Identify the preparation type.
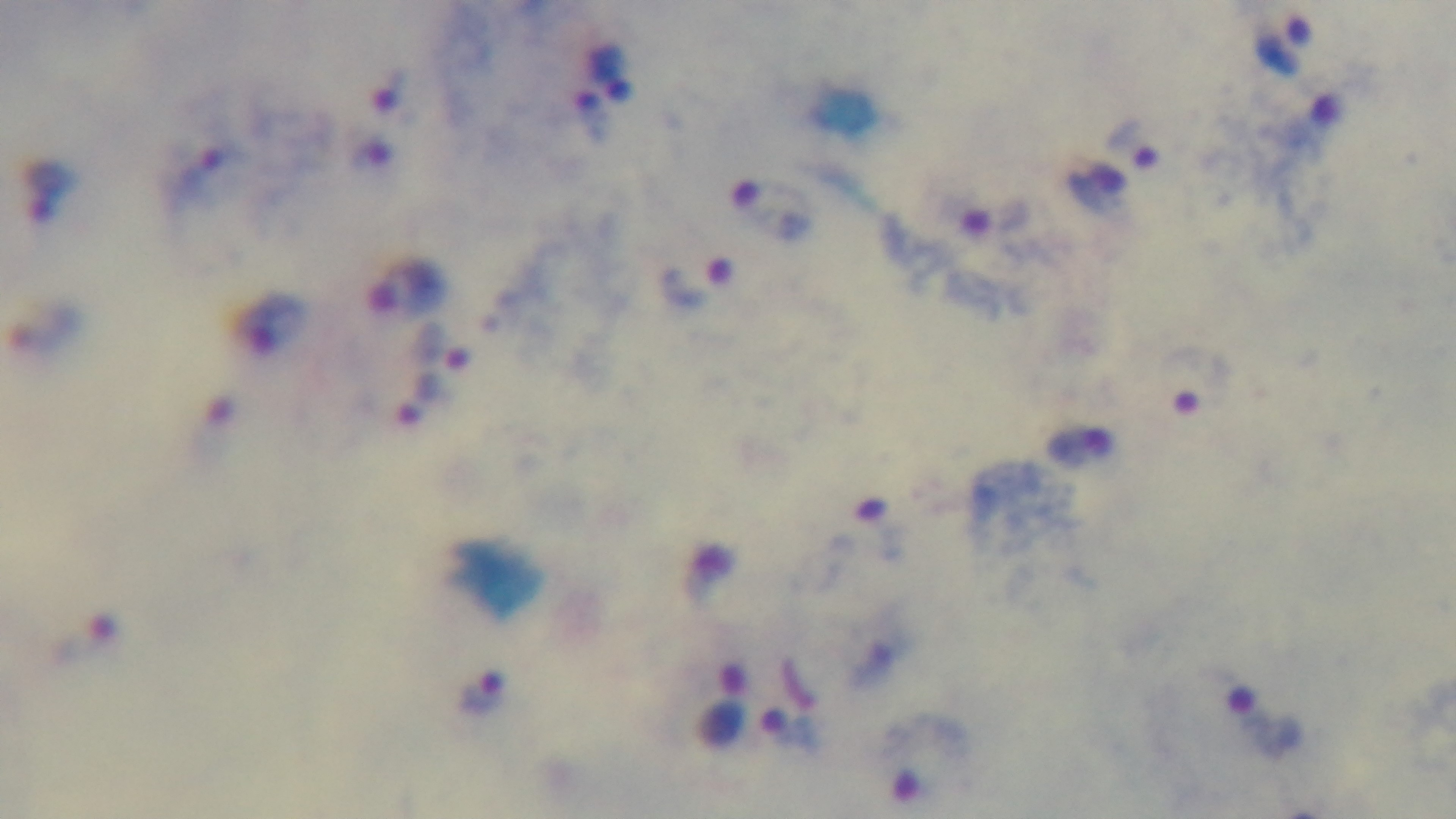
Thick.

100x oil-immersion objective. Light microscopy. Giemsa stain. One field from the slide. Malaria status: positive. Mounted 4K digital camera.